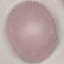

Malaria status: uninfected. Thin blood film. Photographed with a smartphone camera at the microscope eyepiece. Cell patch, automatically extracted from a larger field of view and resized to 64 × 64 pixels. Giemsa-stained preparation.